Locate every blood parasite and identify its species.
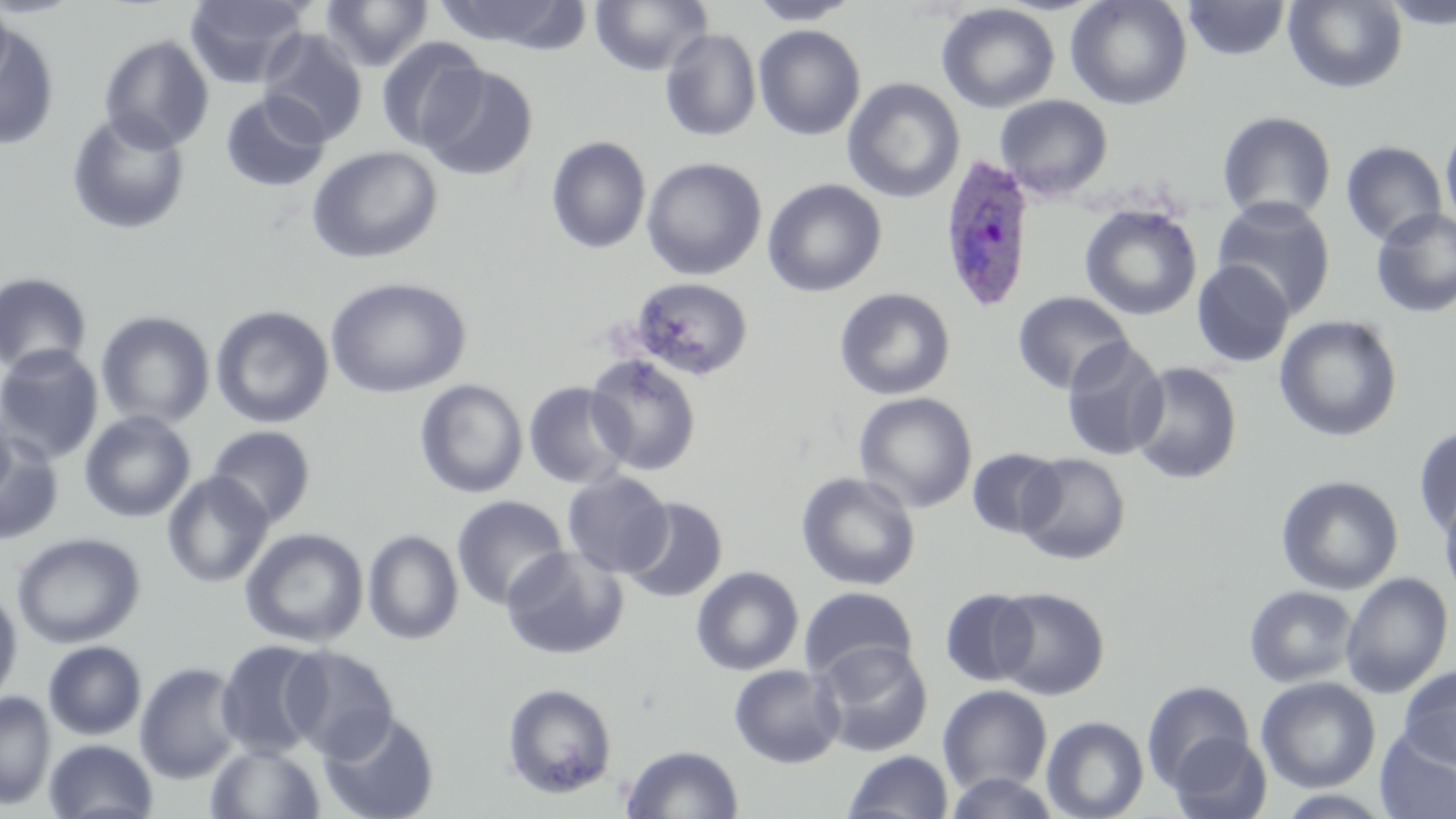
Approximate bounding boxes as (x1, y1, x2, y2) in pixels.
Plasmodium ovale-infected red blood cells: (939, 154, 1035, 313).
No Plasmodium falciparum, Plasmodium malariae, Plasmodium vivax, Babesia divergens, or Trypanosoma brucei observed.

Summary:
  - Uninfected red blood cell locations: (0, 0, 85, 18), (0, 0, 15, 95), (183, 0, 311, 89), (319, 0, 434, 71), (433, 0, 585, 52), (590, 0, 711, 76), (746, 0, 860, 25), (1065, 0, 1192, 111), (1284, 0, 1408, 93), (1379, 0, 1456, 30), (1183, 1, 1291, 61), (936, 3, 1060, 113), (0, 20, 61, 151), (753, 24, 866, 141), (659, 28, 761, 141), (258, 29, 369, 146), (99, 35, 215, 153), (375, 37, 487, 152), (419, 64, 539, 181), (842, 77, 965, 203), (219, 91, 331, 193), (994, 94, 1113, 200), (1216, 110, 1337, 224), (66, 111, 191, 236), (1441, 122, 1456, 235), (546, 136, 651, 254), (1341, 140, 1448, 247), (307, 146, 443, 264), (641, 157, 767, 281), (762, 179, 887, 297), (1211, 196, 1337, 319), (1080, 204, 1202, 321), (1370, 207, 1456, 318), (1191, 260, 1295, 367), (0, 271, 93, 376), (324, 277, 472, 399), (629, 277, 754, 381), (833, 287, 955, 400), (1012, 291, 1133, 395), (209, 299, 472, 420), (210, 304, 334, 429), (95, 310, 215, 429), (1274, 314, 1403, 442), (1060, 336, 1171, 461), (0, 344, 104, 464), (584, 352, 702, 476), (1126, 361, 1243, 485), (414, 379, 527, 500), (522, 381, 633, 489), (853, 392, 978, 513), (0, 406, 16, 506), (79, 411, 195, 523), (1412, 424, 1456, 537), (204, 425, 316, 528), (0, 429, 65, 546), (966, 447, 1065, 539), (1016, 452, 1131, 565), (562, 470, 674, 578), (161, 472, 273, 588), (795, 472, 921, 591), (1276, 474, 1404, 595), (1438, 488, 1456, 604), (451, 495, 568, 610), (622, 497, 728, 603), (240, 527, 368, 647), (362, 529, 463, 645), (11, 532, 145, 649), (500, 546, 628, 660), (691, 565, 804, 676), (1340, 572, 1453, 698), (0, 585, 23, 707), (1243, 585, 1359, 687), (798, 586, 918, 684), (990, 586, 1110, 700), (940, 588, 1038, 687), (215, 639, 330, 759), (43, 640, 147, 740), (812, 640, 933, 757), (280, 645, 398, 761), (134, 661, 244, 783), (728, 664, 844, 768), (1399, 664, 1456, 768), (1255, 676, 1381, 793), (1141, 679, 1255, 791), (502, 682, 618, 799), (937, 685, 1053, 795), (0, 690, 55, 809), (318, 710, 440, 819), (1040, 715, 1149, 819), (1375, 725, 1456, 819), (1168, 732, 1272, 819), (43, 739, 158, 819), (206, 743, 325, 819), (621, 744, 744, 819), (843, 750, 954, 819), (944, 772, 1061, 818), (1274, 789, 1398, 818)
  - Slide-level diagnosis: Plasmodium ovale
  - Modality: light microscopy
  - Field of view: one of a larger specimen
  - Stain: May-Grünwald-Giemsa
  - Image size: 1456×819 pixels
  - Magnification: 1000x
  - Preparation: thin blood film